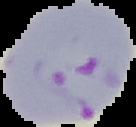

{
  "preparation": "thin blood film",
  "image_size": "136×127 pixels",
  "malaria_status": "parasitized",
  "image_type": "segmented cell region on a black background"
}